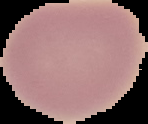

Summary:
  - Image type: segmented cell region with the area outside set to black
  - Malaria status: uninfected
  - Preparation: thin blood smear
  - Image size: 148×124 pixels